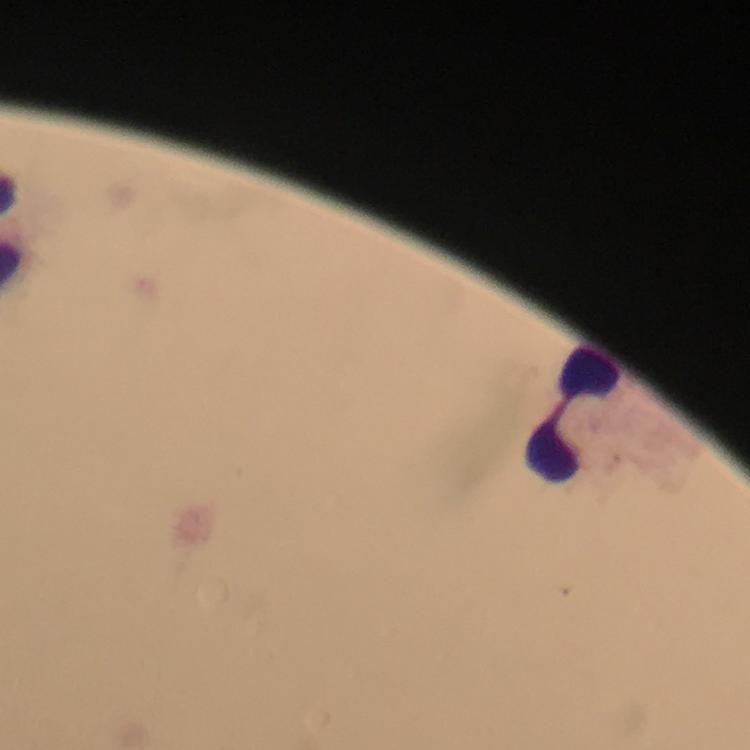
capture = smartphone photograph through a microscope
magnification = 100x
preparation = thick smear
Plasmodium parasites = none seen
stain = Giemsa
leukocyte locations = approximate centers as {x, y} in pixels: {576, 415}
cropped from = a single field of view
image size = 750×750 pixels
context = from a malaria diagnostic workup
immersion oil = used